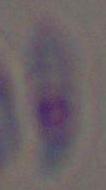

magnification = 1000x
modality = micrograph
identification = Toxoplasma gondii